Assess this cell for malaria.
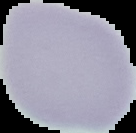

Uninfected.

The area outside the segmented cell region is set to black. From a thin blood film. Image is 136×133 pixels.